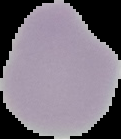
malaria status = uninfected
image type = segmented cell region on a black background
image size = 121×139 pixels
preparation = thin blood film